Report the malaria status of this cell.
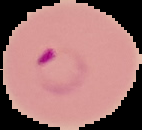
It is parasitized.

preparation = thin blood smear
image size = 142×130 pixels
image type = segmented cell region with the area outside set to black